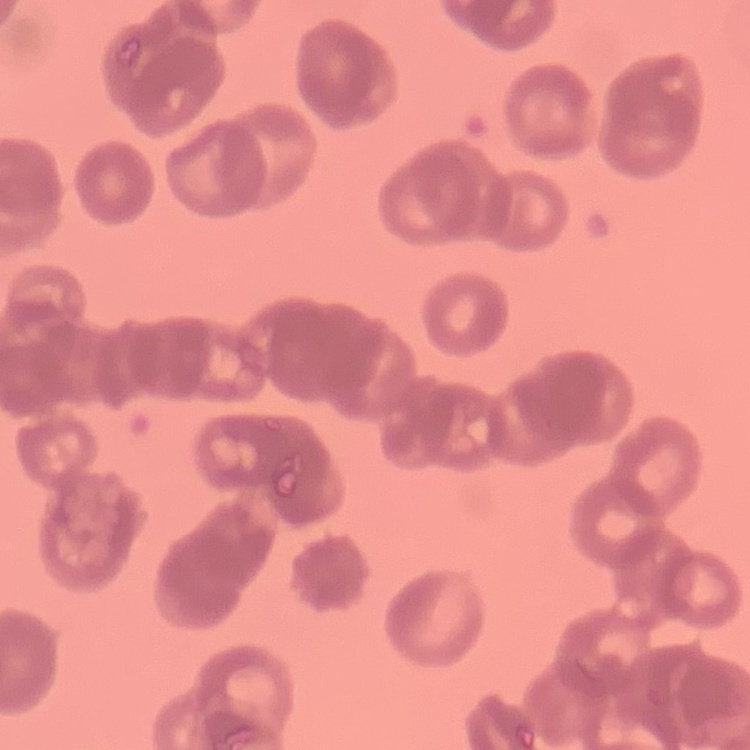

Summary:
  - Erythrocyte morphology: rouleaux formation
  - Image type: square crop of a larger photomicrograph
  - Preparation: thin blood smear
  - Stain: Field's or Giemsa